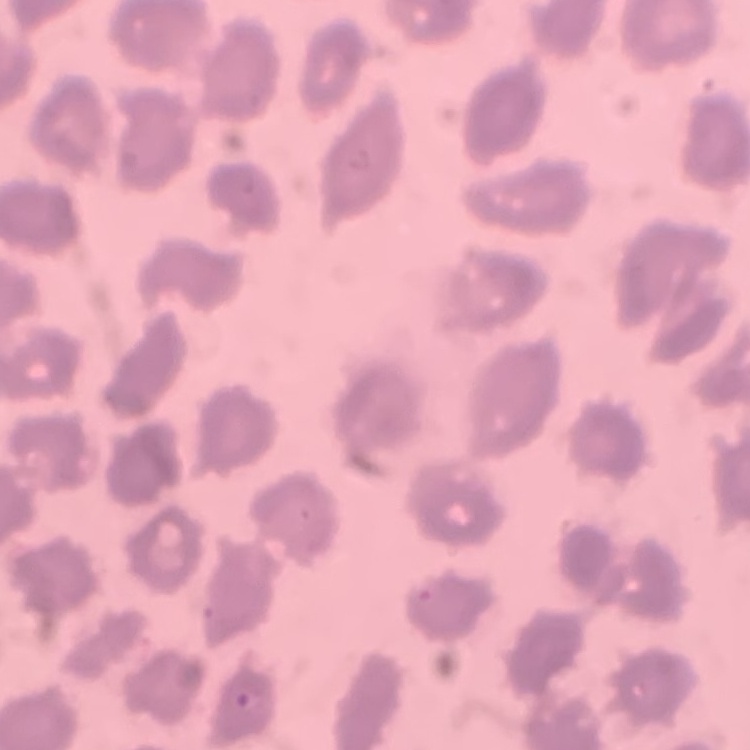

Summary:
  - Erythrocyte morphology: no rouleaux formation
  - Image type: square crop of a larger photomicrograph
  - Stain: Field's or Giemsa
  - Preparation: thin peripheral smear